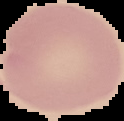
preparation: thin blood smear
image_size: 124×121 pixels
image_type: segmented cell region with the area outside set to black
result: negative for Plasmodium parasites